Give the position of every leukocyte visible.
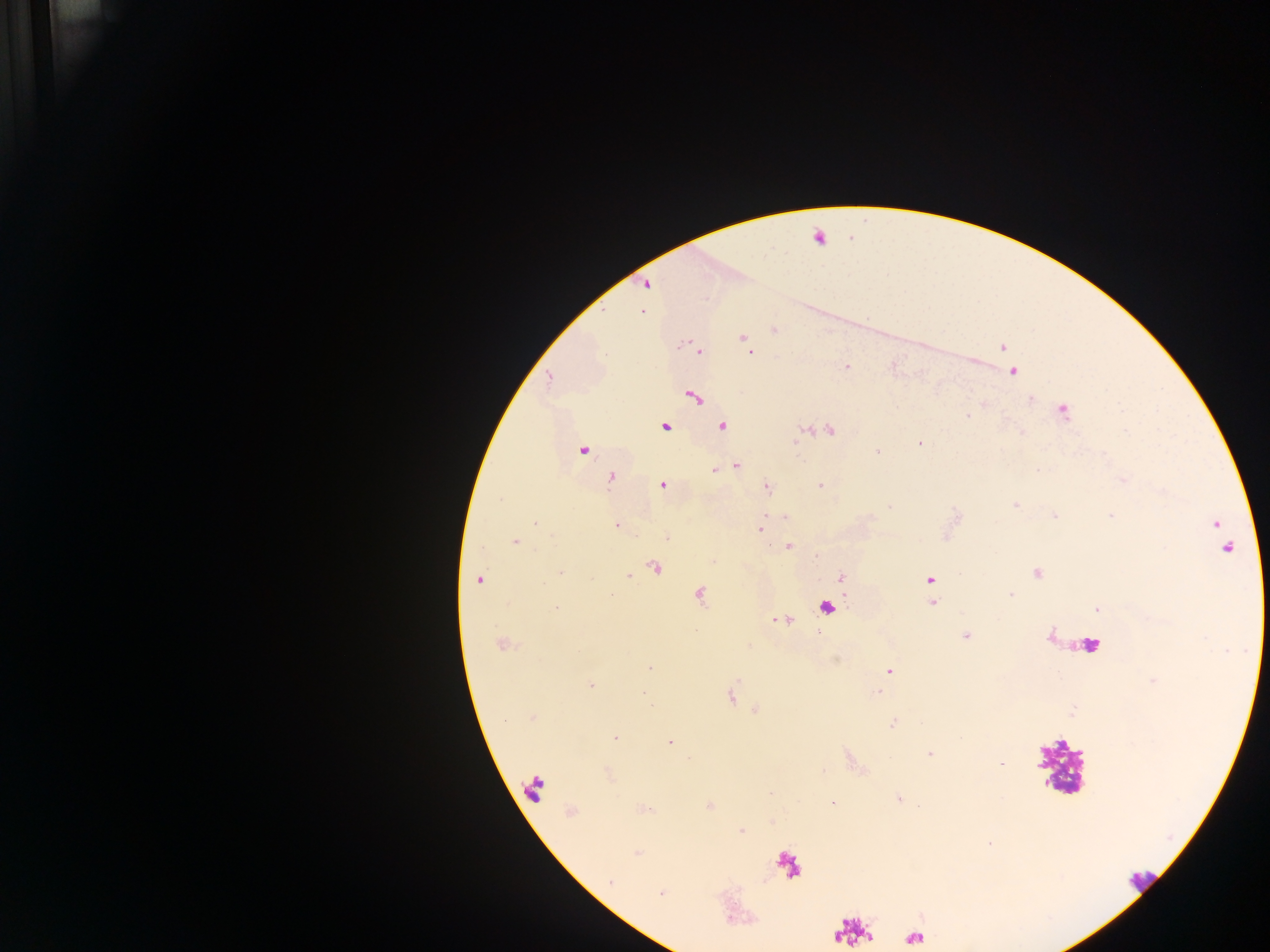
Approximate centers as [x, y] in pixels.
Leukocytes: [822, 233], [827, 608], [1091, 643], [1060, 767], [535, 788], [1141, 880].

capture = mobile-phone photograph through a microscope
country = Ghana
Plasmodium parasite locations = approximate centers as [x, y] in pixels: [646, 284], [643, 311], [774, 330], [743, 338], [1002, 348], [699, 351], [749, 352], [847, 366], [1013, 372], [549, 378], [694, 397], [1031, 399], [1062, 411], [968, 416], [665, 426], [722, 426], [830, 431], [920, 443], [582, 450], [876, 452], [736, 465], [715, 471], [611, 478], [662, 485], [820, 485], [767, 488], [1014, 505], [1054, 515], [784, 517], [535, 523], [1217, 524], [617, 525], [760, 529], [667, 538], [516, 541], [789, 546], [1225, 546], [655, 568], [560, 571], [1036, 573], [629, 576], [841, 577], [479, 579], [929, 579], [1010, 594], [699, 596], [932, 603], [555, 609], [1096, 609], [966, 636], [502, 645], [649, 668], [889, 671], [590, 685], [878, 692], [643, 693], [532, 717], [893, 723], [615, 737], [669, 742], [929, 754], [1001, 764], [899, 799], [833, 802], [742, 831], [637, 853], [611, 881], [661, 894]
field of view = single
preparation = thick blood smear
image size = 1270×952 pixels